Assess this cell for malaria.
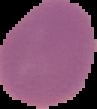
Uninfected.

{
  "image_size": "97×109 pixels",
  "image_type": "cell region segmented out of the field of view; surrounding area masked to black",
  "preparation": "thin blood film"
}